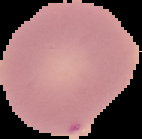 Malaria status: uninfected. From a thin blood film. Image is 142×139 pixels. Segmented cell region on a black background.